Identify the cell.
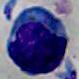
A leukocyte.

Summary:
  - Magnification: 1000x
  - Modality: micrograph